Classify this cell by malaria status.
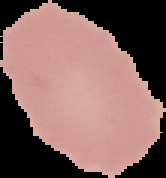
It is uninfected.

image size = 166×178 pixels
image type = cell region segmented out of the field of view; surrounding area masked to black
preparation = thin blood film